Describe the morphology of the red blood cells.
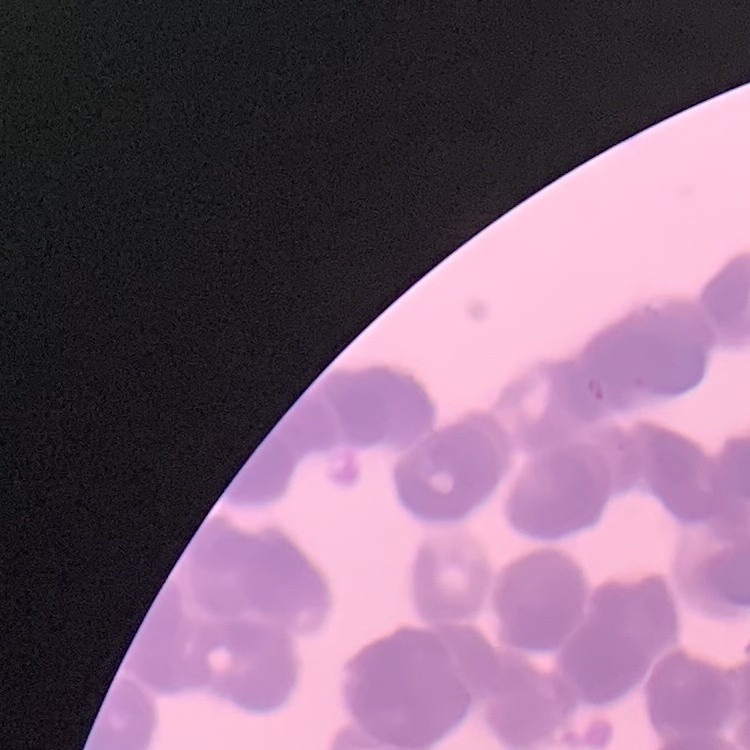

They show rouleaux formation.

{
  "preparation": "thin blood smear",
  "stain": "Field's or Giemsa",
  "image_type": "one tile cut from a larger photomicrograph"
}